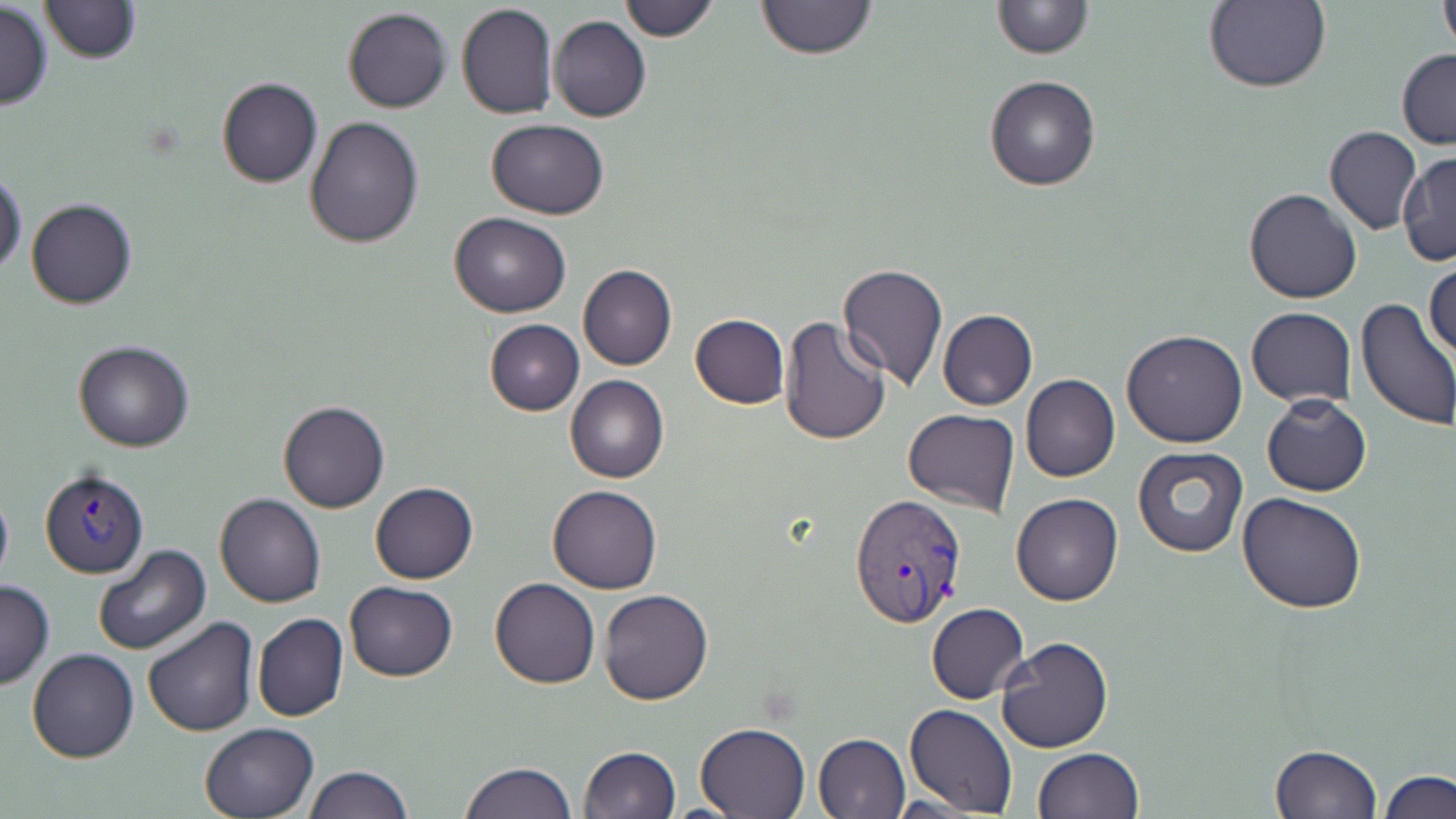
Summary:
  - Coordinate format: approximate bounding boxes as [x1, y1, x2, y2] in pixels
  - Plasmodium vivax-infected red blood cell locations: [40, 469, 149, 579], [848, 492, 966, 628]
  - Uninfected red blood cell locations: [39, 0, 140, 64], [618, 0, 719, 40], [753, 0, 881, 61], [990, 0, 1092, 58], [1202, 1, 1332, 94], [456, 2, 559, 120], [1438, 3, 1456, 54], [0, 4, 54, 109], [342, 7, 451, 112], [548, 15, 652, 122], [1397, 48, 1456, 149], [984, 75, 1101, 191], [215, 78, 323, 188], [305, 115, 423, 249], [485, 119, 612, 218], [1323, 125, 1423, 236], [1398, 151, 1455, 267], [0, 170, 27, 279], [1244, 187, 1362, 305], [25, 197, 137, 310], [450, 211, 570, 318], [1424, 258, 1455, 362], [837, 262, 949, 391], [578, 264, 676, 372], [1354, 297, 1456, 432], [1247, 307, 1357, 406], [938, 309, 1038, 410], [690, 313, 790, 409], [778, 316, 890, 446], [483, 319, 584, 416], [1122, 329, 1248, 448], [73, 340, 195, 452], [1021, 374, 1120, 482], [565, 375, 668, 484], [1261, 394, 1371, 496], [277, 401, 389, 513], [902, 410, 1019, 516], [1132, 446, 1250, 559], [369, 482, 478, 583], [0, 483, 12, 591], [548, 485, 661, 595], [1237, 491, 1367, 612], [1011, 492, 1122, 605], [214, 493, 325, 608], [92, 544, 211, 656], [490, 577, 600, 688], [0, 579, 53, 689], [344, 581, 457, 681], [598, 589, 713, 705], [926, 603, 1029, 703], [252, 613, 348, 724], [141, 616, 260, 739], [995, 636, 1112, 753], [27, 649, 140, 764], [904, 703, 1018, 817], [695, 720, 810, 818], [200, 721, 320, 819], [811, 733, 910, 819], [1267, 744, 1381, 819], [578, 746, 681, 819], [1033, 747, 1143, 818], [460, 761, 578, 818], [302, 764, 413, 819], [1380, 769, 1455, 819]
  - Slide-level diagnosis: Plasmodium vivax
  - Magnification: 1000x
  - Field of view: one of a larger specimen
  - Image size: 1456×819 pixels
  - Preparation: thin blood film
  - Modality: light microscopy
  - Stain: May-Grünwald-Giemsa